Locate and identify every blood parasite.
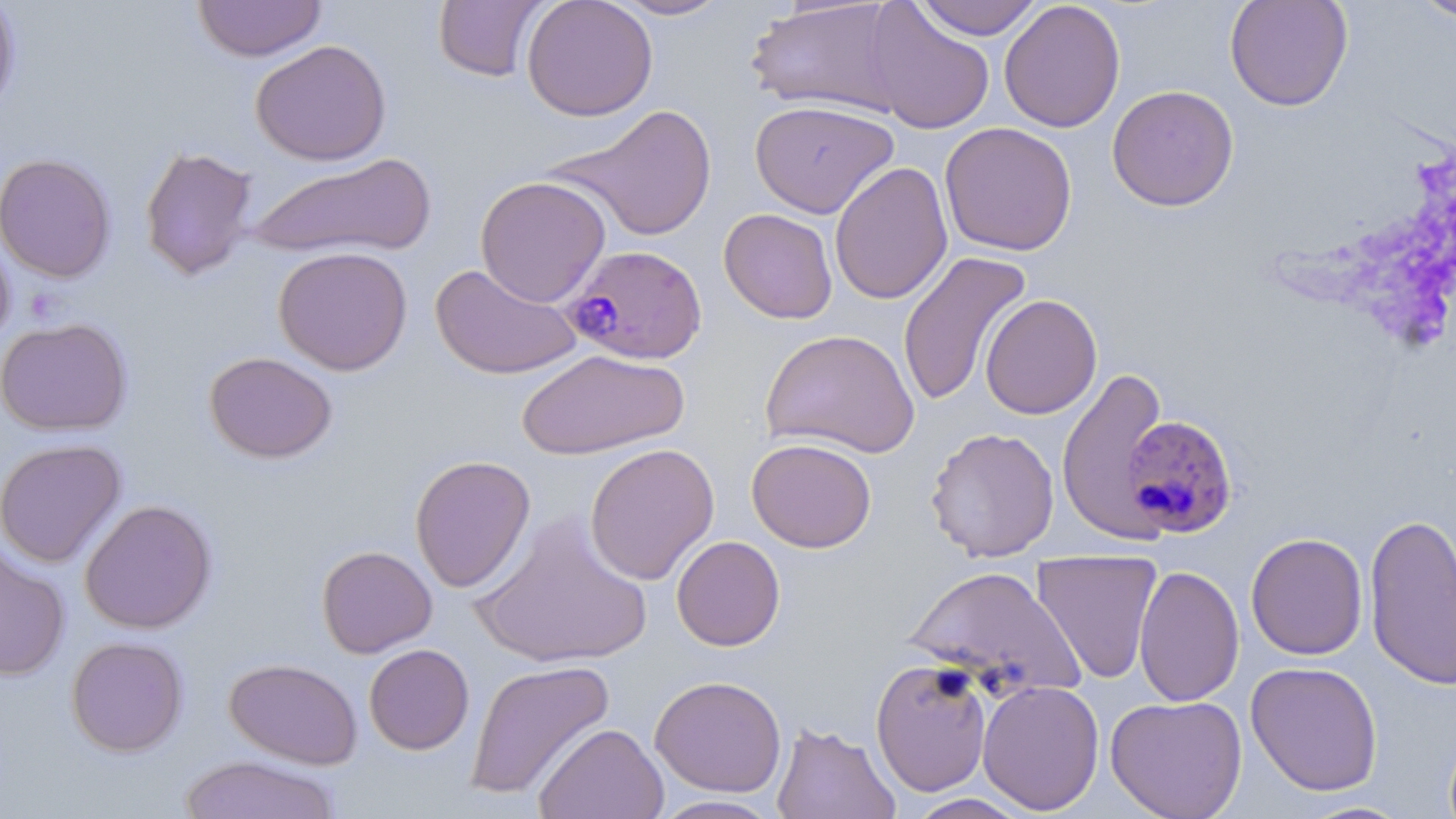

Approximate bounding boxes as (x1,y1)-(x2,y2) corner pairs in pixels.
Plasmodium falciparum-infected red blood cells: (561,243)-(708,365), (1120,414)-(1239,539).
No Plasmodium ovale, Plasmodium malariae, Plasmodium vivax, Babesia divergens, or Trypanosoma brucei observed.

slide_level_diagnosis: Plasmodium falciparum
field_of_view: one of a larger specimen
modality: light microscopy
uninfected_red_blood_cell_locations: 'approximate bounding boxes as (x1,y1)-(x2,y2) corner pairs in pixels: (0,0)-(21,117), (192,0)-(327,62), (433,0)-(548,82), (521,0)-(658,121), (609,0)-(732,20), (912,0)-(1044,40), (1224,0)-(1353,111), (1411,0)-(1456,24), (745,1)-(906,117), (999,1)-(1126,133), (862,2)-(995,135), (250,39)-(392,166), (1106,84)-(1239,211), (750,99)-(899,218), (548,103)-(719,242), (940,122)-(1077,256), (139,145)-(258,280), (243,151)-(437,263), (0,152)-(116,283), (829,161)-(953,305), (475,175)-(611,307), (718,209)-(838,324), (0,229)-(16,351), (273,246)-(413,375), (897,250)-(1033,408), (430,263)-(582,380), (980,294)-(1102,420), (0,317)-(132,436), (760,328)-(920,459), (517,348)-(689,460), (204,351)-(338,463), (1057,366)-(1170,543), (925,426)-(1060,562), (0,438)-(126,567), (746,438)-(877,553), (584,442)-(720,585), (410,454)-(536,593), (79,498)-(217,634), (471,510)-(653,671), (1363,512)-(1455,692), (1245,532)-(1368,660), (671,535)-(785,651), (0,544)-(70,681), (316,545)-(437,658), (1031,549)-(1163,685), (903,564)-(1085,702), (1134,564)-(1245,707), (66,636)-(189,757), (364,643)-(474,755), (224,657)-(362,770), (466,658)-(616,800), (870,658)-(993,796), (1245,660)-(1384,796), (650,675)-(787,797), (978,679)-(1105,815), (1105,694)-(1247,819), (771,722)-(900,819), (534,723)-(669,819), (178,755)-(341,818), (903,793)-(1033,818), (649,795)-(786,818), (1298,800)-(1414,818)'
image_size: 1456×819 pixels
preparation: thin blood film
magnification: 1000x
stain: May-Grünwald-Giemsa